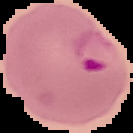

preparation = thin blood film
malaria status = parasitized
image type = segmented cell region on a black background
image size = 133×133 pixels